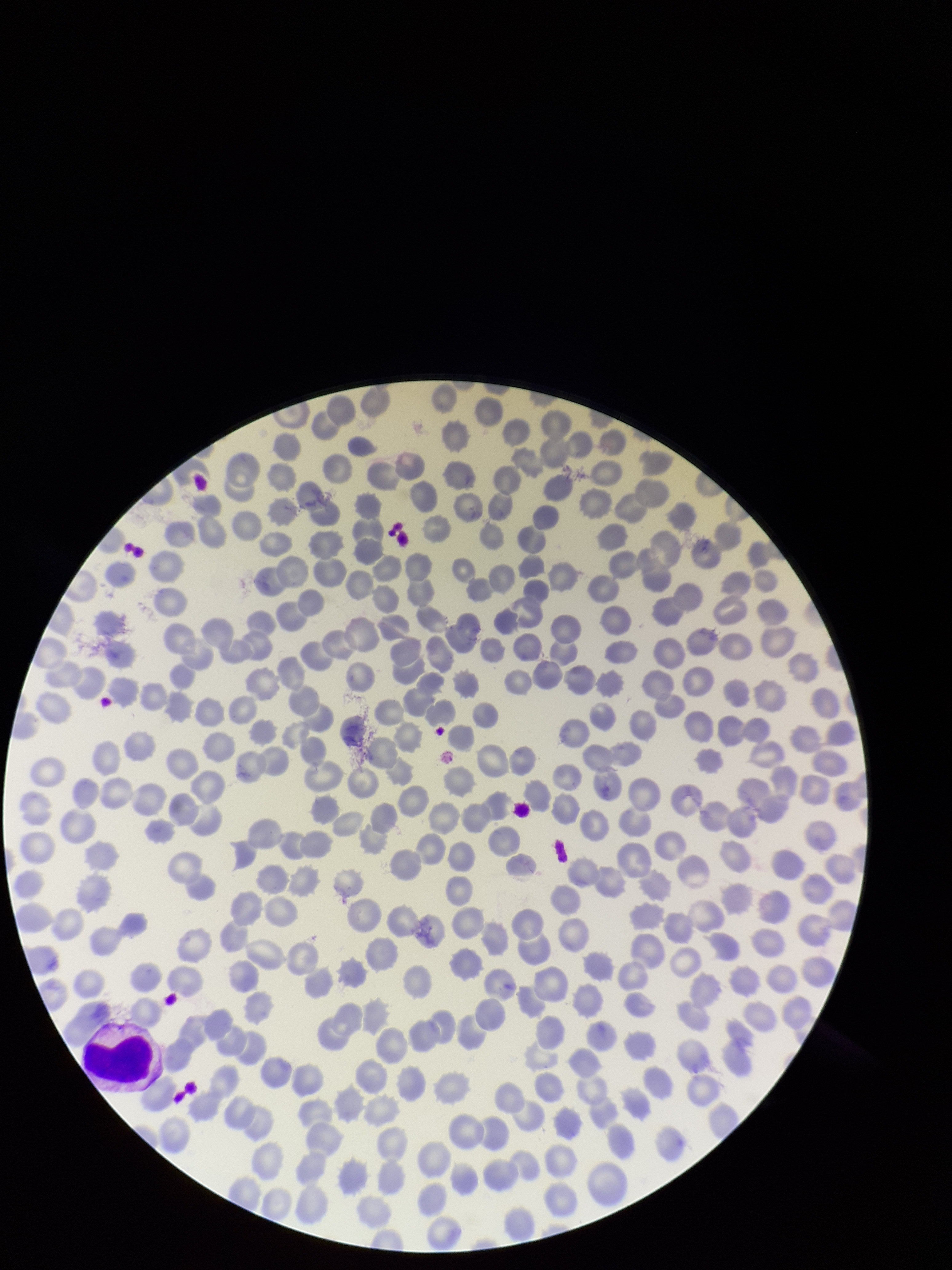
Summary:
  - Patient malaria status: positive
  - Field of view: one from this slide
  - Red blood cell count: 239
  - Parasitized red blood cell count: 0
  - Image size: 952×1270 pixels
  - Parasitized red blood cells: none identified
  - Stain: Giemsa
  - Capture: smartphone photograph through the microscope eyepiece
  - Species reported for this patient: Plasmodium falciparum
  - Preparation: thin smear